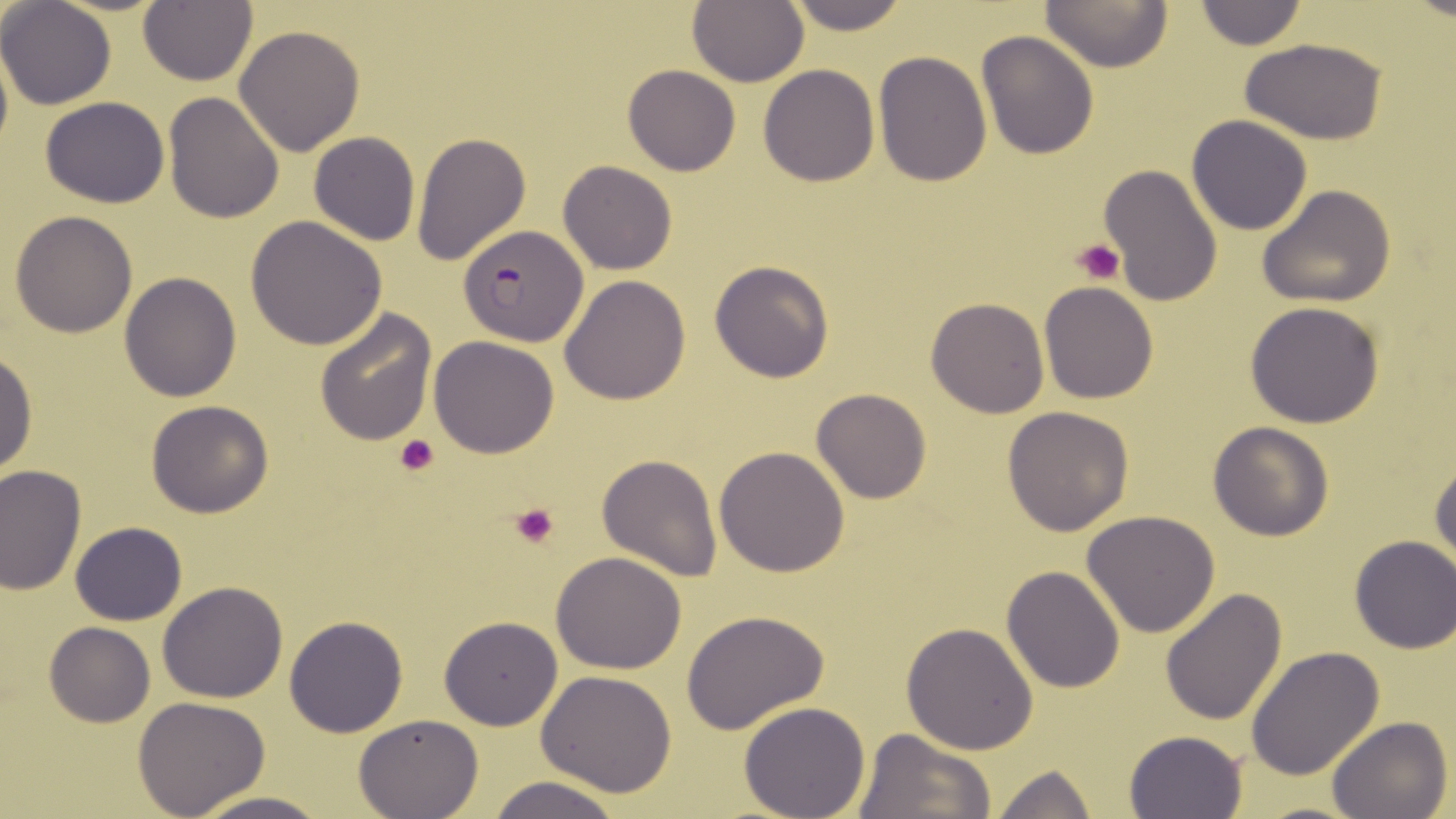
slide_level_diagnosis: Plasmodium falciparum
field_of_view: single
image_size: 1456×819 pixels
platelet_locations: 'approximate bounding boxes as [x1, y1, x2, y2] in pixels: [1074, 239, 1124, 285], [393, 434, 439, 477], [511, 503, 559, 549]'
magnification: 1000x
plasmodium_falciparum_infected_red_blood_cell_locations: 'approximate bounding boxes as [x1, y1, x2, y2] in pixels: [458, 227, 586, 346]'
uninfected_red_blood_cell_locations: 'approximate bounding boxes as [x1, y1, x2, y2] in pixels: [782, 0, 911, 35], [1040, 0, 1172, 71], [1194, 0, 1308, 51], [1, 1, 117, 110], [686, 2, 808, 87], [138, 3, 258, 86], [233, 24, 366, 156], [976, 30, 1101, 158], [1240, 36, 1390, 145], [873, 52, 992, 186], [624, 64, 741, 176], [758, 64, 881, 186], [163, 92, 284, 225], [40, 96, 170, 207], [1186, 115, 1313, 236], [308, 131, 421, 246], [410, 131, 532, 268], [557, 161, 676, 276], [1098, 164, 1224, 307], [1257, 184, 1396, 308], [10, 210, 138, 337], [245, 217, 388, 353], [708, 260, 834, 383], [120, 272, 241, 402], [559, 275, 691, 406], [1040, 282, 1159, 404], [927, 300, 1049, 417], [1243, 301, 1387, 428], [314, 309, 436, 447], [430, 335, 561, 458], [0, 348, 38, 477], [811, 389, 932, 504], [146, 399, 274, 518], [1002, 406, 1133, 537], [1207, 420, 1335, 540], [715, 446, 849, 576], [597, 452, 724, 582], [1430, 456, 1455, 570], [0, 466, 86, 592], [1082, 510, 1219, 637], [70, 521, 186, 626], [1350, 535, 1456, 654], [551, 551, 689, 675], [1002, 565, 1126, 694], [157, 580, 288, 703], [1160, 588, 1288, 726], [682, 608, 831, 736], [284, 615, 409, 738], [439, 615, 563, 731], [43, 621, 155, 727], [901, 621, 1040, 755], [1246, 645, 1386, 780], [535, 670, 678, 796], [133, 696, 270, 818], [738, 700, 871, 819], [355, 714, 483, 819], [1327, 716, 1455, 819], [851, 729, 993, 819], [1124, 729, 1247, 817], [991, 762, 1097, 819], [488, 775, 623, 819], [190, 792, 330, 819]'
modality: light microscopy
stain: May-Grünwald-Giemsa
preparation: thin blood smear